Name the parasite shown.
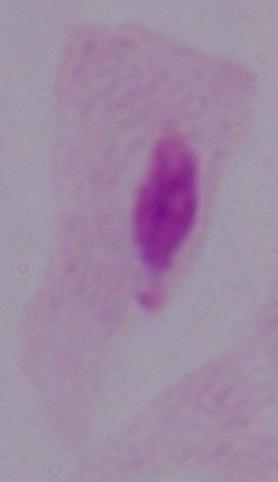
This is a trichomonad.

Summary:
  - Modality: micrograph
  - Magnification: 1000x